Outline each uninfected red blood cell.
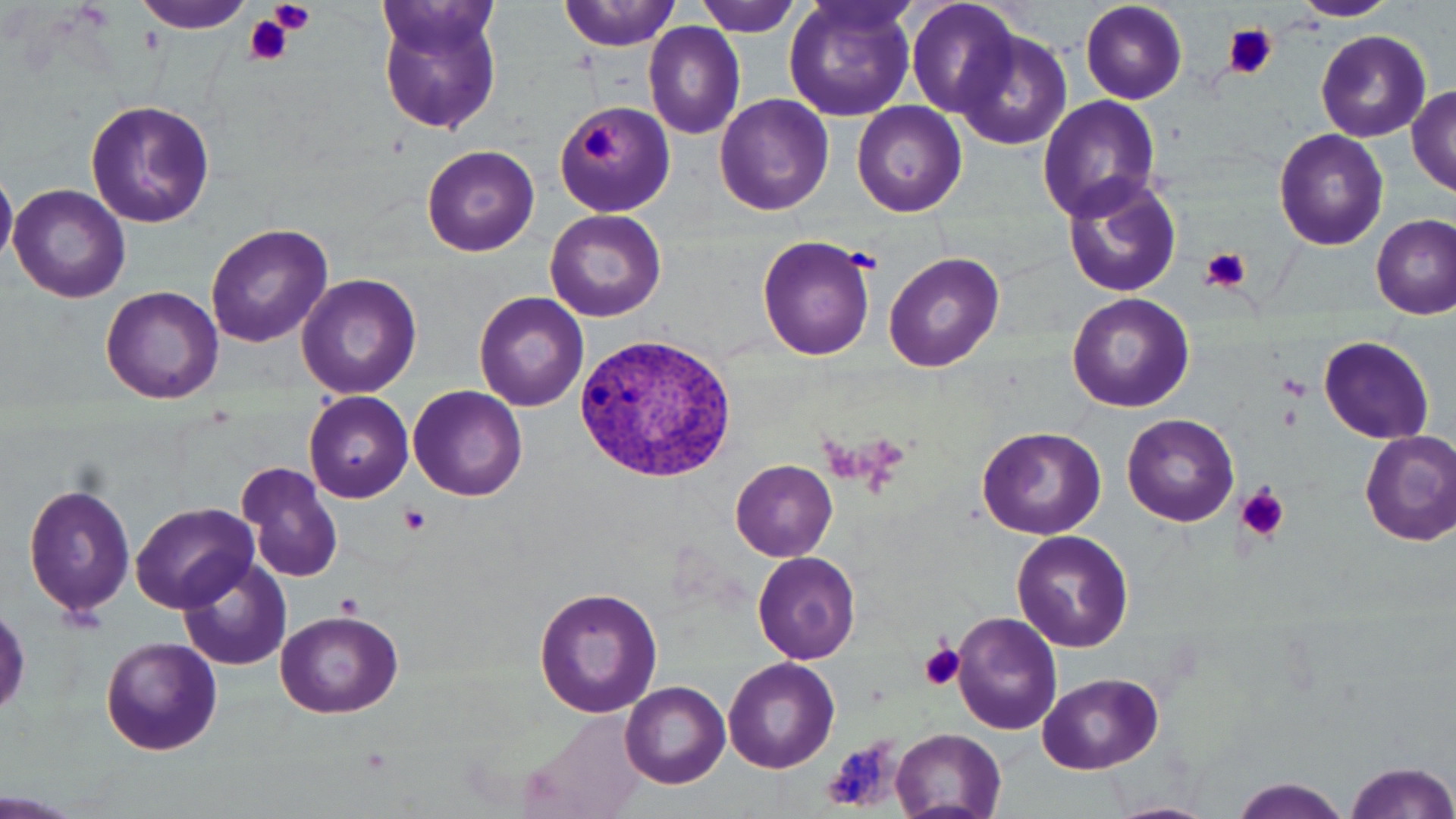

Approximate bounding boxes as (x1, y1, x2, y2) in pixels.
Uninfected red blood cells: (373, 0, 507, 138), (904, 0, 1024, 119), (1079, 0, 1189, 105), (1291, 0, 1395, 20), (135, 1, 251, 35), (559, 1, 683, 51), (693, 1, 806, 37), (783, 1, 919, 121), (643, 22, 746, 140), (954, 26, 1073, 150), (1317, 29, 1431, 141), (1407, 86, 1456, 194), (714, 94, 834, 216), (1036, 95, 1162, 221), (85, 100, 216, 229), (555, 100, 677, 215), (852, 103, 966, 217), (1273, 128, 1390, 250), (421, 145, 539, 257), (0, 172, 17, 263), (1060, 174, 1183, 298), (8, 183, 131, 302), (545, 209, 666, 322), (1372, 214, 1455, 320), (206, 223, 333, 348), (757, 234, 879, 360), (883, 252, 1003, 372), (295, 274, 421, 400), (99, 285, 222, 403), (475, 291, 589, 412), (1066, 292, 1194, 411), (1318, 334, 1434, 444), (407, 386, 526, 499), (303, 392, 413, 503), (1122, 413, 1240, 527), (977, 426, 1106, 540), (1358, 430, 1456, 544), (731, 460, 838, 561), (240, 462, 344, 585), (21, 478, 138, 619), (132, 503, 258, 612), (1012, 531, 1133, 653), (752, 550, 862, 663), (179, 557, 294, 672), (534, 585, 663, 721), (272, 610, 403, 718), (952, 612, 1062, 735), (100, 636, 224, 757), (723, 657, 840, 772), (1037, 674, 1163, 774), (621, 682, 730, 788), (521, 710, 655, 819), (890, 729, 1007, 818), (1341, 759, 1456, 819), (1228, 778, 1351, 819).

Platelet locations: (269, 0, 316, 34), (244, 14, 296, 66), (1225, 25, 1277, 80), (579, 124, 625, 161), (1200, 246, 1252, 293), (1276, 373, 1311, 397), (1236, 483, 1289, 541), (398, 504, 431, 535), (336, 592, 365, 620), (918, 643, 967, 693), (824, 736, 902, 812). Plasmodium vivax-infected red blood cell locations: (572, 332, 741, 485). Slide-level diagnosis: Plasmodium vivax. Thin blood film. Image is 1456×819 pixels. One field of a larger specimen. Optical microscopy. Captured at 1000x magnification. May-Grünwald-Giemsa stain.